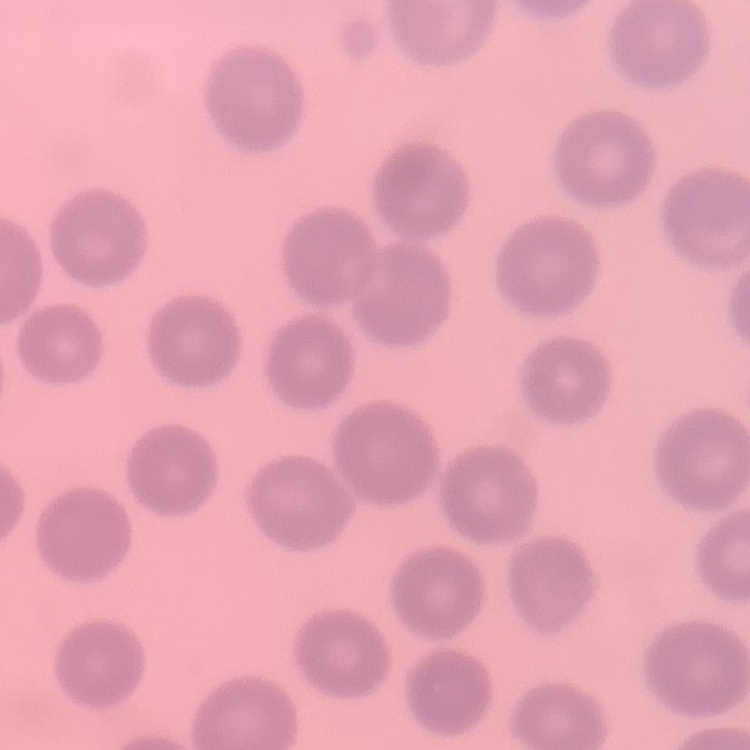 The red blood cells show no rouleaux formation. Field's or Giemsa stain. Thin peripheral smear. Square crop of a larger photomicrograph.